Identify the blood parasite species.
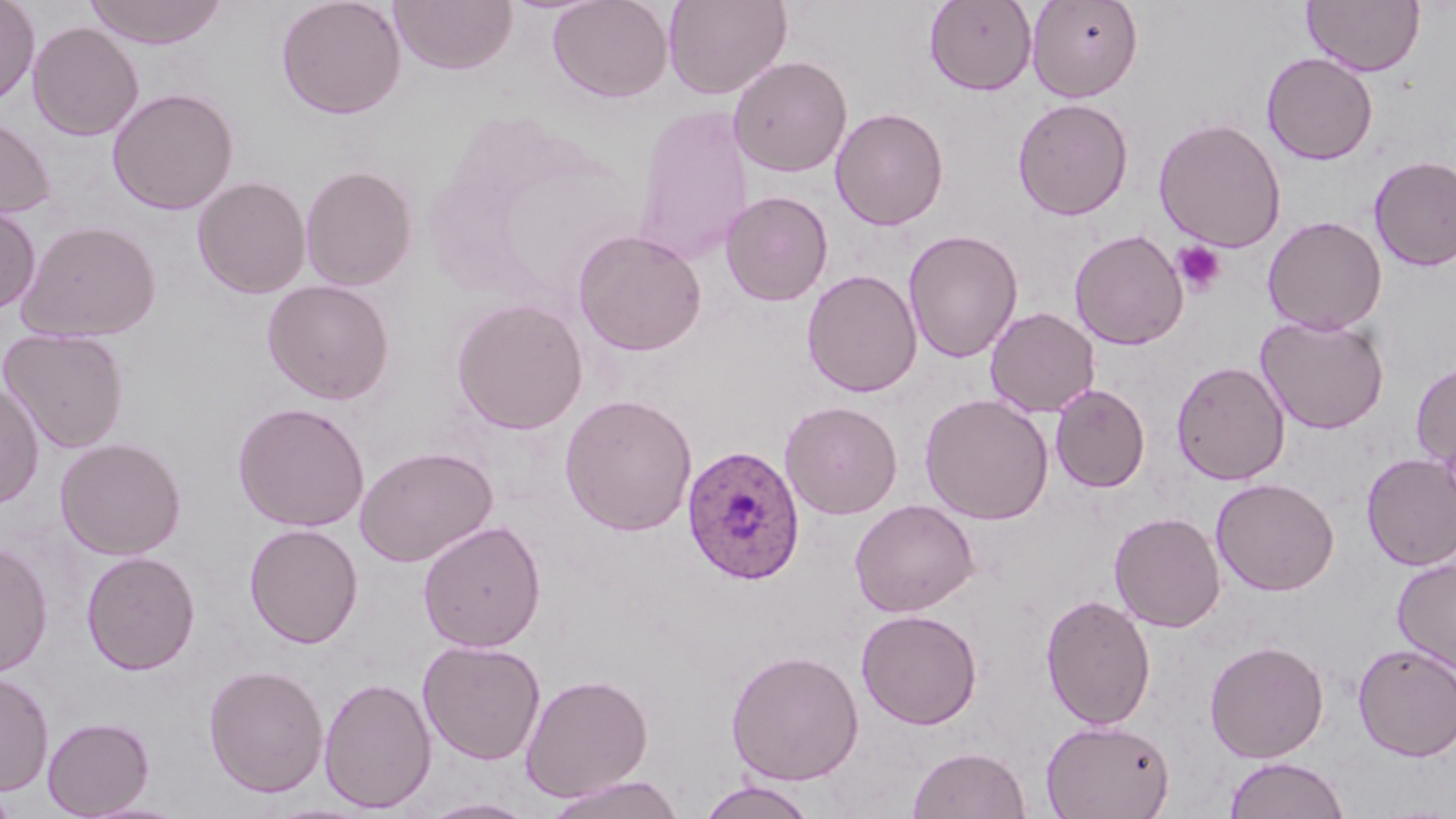

Plasmodium ovale.

Approximate bounding boxes as named x1/y1/x2/y2 corners in pixels. Platelet locations: (x1=1173, y1=240, x2=1227, y2=297). Plasmodium ovale-infected red blood cell locations: (x1=681, y1=443, x2=805, y2=585). Uninfected red blood cell locations: (x1=0, y1=0, x2=39, y2=106), (x1=84, y1=0, x2=228, y2=48), (x1=276, y1=0, x2=406, y2=119), (x1=390, y1=0, x2=517, y2=74), (x1=547, y1=0, x2=673, y2=103), (x1=663, y1=0, x2=792, y2=100), (x1=924, y1=0, x2=1038, y2=95), (x1=1028, y1=0, x2=1143, y2=102), (x1=1302, y1=0, x2=1424, y2=76), (x1=27, y1=21, x2=144, y2=141), (x1=1261, y1=52, x2=1379, y2=165), (x1=727, y1=54, x2=852, y2=178), (x1=107, y1=88, x2=239, y2=215), (x1=1012, y1=97, x2=1133, y2=221), (x1=633, y1=105, x2=755, y2=265), (x1=830, y1=107, x2=949, y2=230), (x1=0, y1=115, x2=56, y2=220), (x1=1153, y1=117, x2=1287, y2=252), (x1=1369, y1=154, x2=1456, y2=272), (x1=300, y1=165, x2=418, y2=291), (x1=191, y1=175, x2=311, y2=299), (x1=720, y1=191, x2=833, y2=307), (x1=0, y1=202, x2=41, y2=314), (x1=1263, y1=215, x2=1387, y2=335), (x1=16, y1=219, x2=162, y2=343), (x1=572, y1=229, x2=707, y2=356), (x1=903, y1=229, x2=1023, y2=364), (x1=1069, y1=229, x2=1189, y2=350), (x1=801, y1=268, x2=923, y2=398), (x1=261, y1=279, x2=396, y2=405), (x1=450, y1=297, x2=588, y2=435), (x1=986, y1=307, x2=1100, y2=418), (x1=1256, y1=314, x2=1389, y2=433), (x1=1, y1=328, x2=129, y2=454), (x1=1171, y1=360, x2=1290, y2=486), (x1=1411, y1=360, x2=1456, y2=476), (x1=0, y1=381, x2=44, y2=510), (x1=1050, y1=384, x2=1150, y2=493), (x1=919, y1=392, x2=1054, y2=525), (x1=559, y1=393, x2=698, y2=536), (x1=780, y1=400, x2=903, y2=519), (x1=232, y1=401, x2=370, y2=532), (x1=55, y1=437, x2=187, y2=560), (x1=354, y1=445, x2=498, y2=567), (x1=1360, y1=452, x2=1456, y2=570), (x1=1211, y1=477, x2=1340, y2=595), (x1=849, y1=498, x2=979, y2=617), (x1=1109, y1=511, x2=1226, y2=632), (x1=418, y1=519, x2=546, y2=653), (x1=244, y1=523, x2=364, y2=649), (x1=0, y1=542, x2=54, y2=678), (x1=81, y1=550, x2=200, y2=675), (x1=1392, y1=556, x2=1456, y2=674), (x1=1040, y1=593, x2=1157, y2=730), (x1=856, y1=608, x2=983, y2=729), (x1=417, y1=639, x2=546, y2=765), (x1=1205, y1=640, x2=1329, y2=763), (x1=1352, y1=642, x2=1456, y2=761), (x1=726, y1=649, x2=864, y2=785), (x1=203, y1=664, x2=328, y2=798), (x1=0, y1=671, x2=54, y2=797), (x1=520, y1=673, x2=653, y2=801), (x1=319, y1=676, x2=437, y2=813), (x1=42, y1=716, x2=155, y2=818), (x1=1040, y1=718, x2=1176, y2=819), (x1=907, y1=745, x2=1031, y2=819), (x1=1224, y1=756, x2=1350, y2=819), (x1=545, y1=774, x2=686, y2=819), (x1=696, y1=778, x2=821, y2=819), (x1=419, y1=797, x2=540, y2=818), (x1=77, y1=799, x2=196, y2=819). Light microscopy. May-Grünwald-Giemsa-stained preparation. Captured at 1000x magnification. Single field of view. Thin blood film. Image is 1456×819 pixels.